Give the extent of all Plasmodium malariae-infected red blood cells.
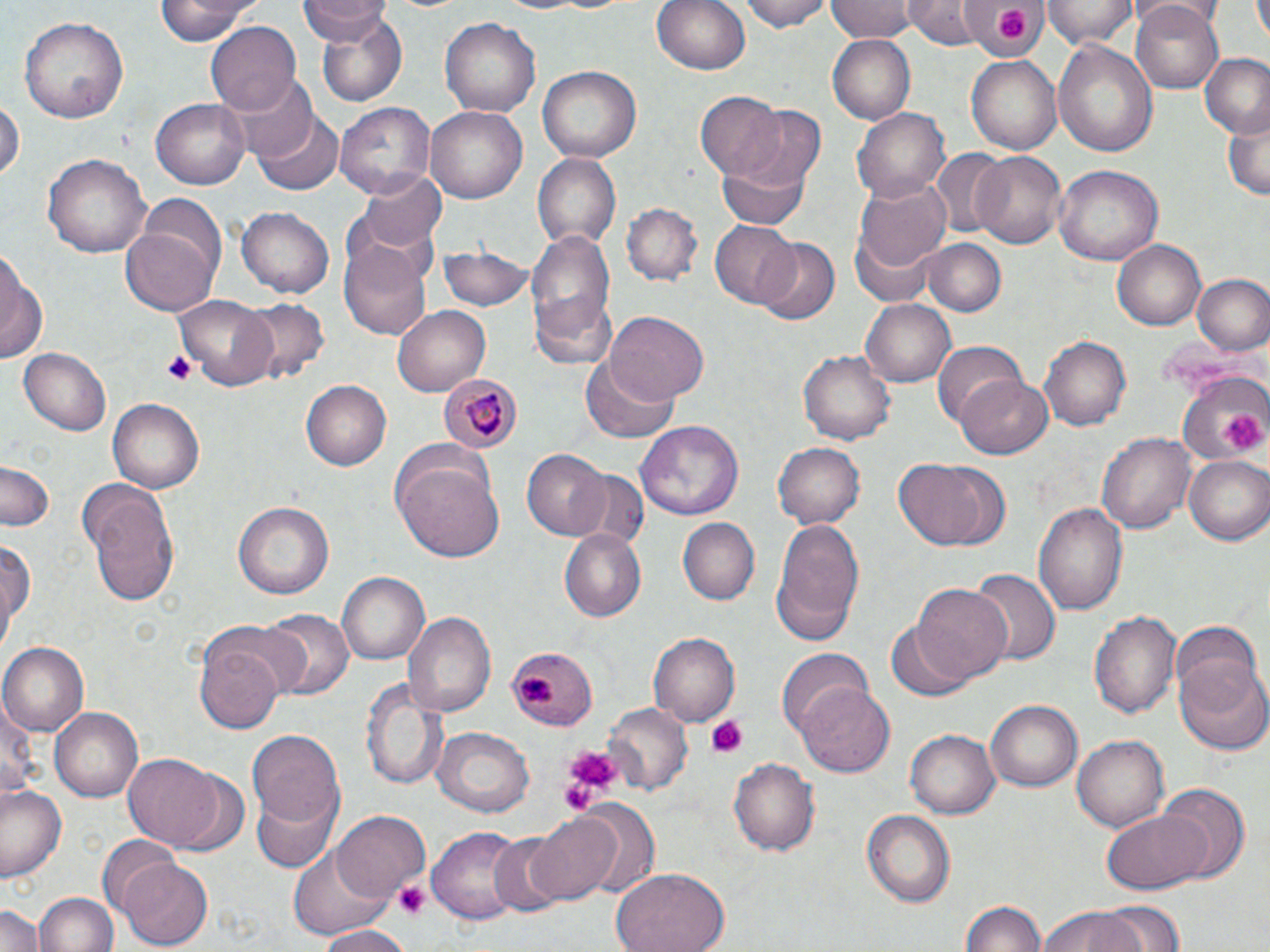
Approximate bounding boxes as [x1, y1, x2, y2] in pixels.
Plasmodium malariae-infected red blood cells: [441, 371, 521, 455].

Platelet locations: [992, 6, 1028, 43], [161, 350, 195, 386], [1220, 409, 1266, 454], [516, 674, 559, 711], [704, 716, 748, 757], [561, 744, 619, 797], [558, 764, 606, 816], [395, 882, 428, 920]. Uninfected red blood cell locations: [154, 0, 263, 46], [298, 0, 389, 41], [654, 0, 752, 76], [741, 0, 833, 31], [826, 0, 916, 43], [906, 0, 982, 46], [1043, 0, 1135, 49], [959, 2, 1050, 60], [1252, 2, 1270, 41], [1132, 3, 1224, 91], [313, 10, 407, 108], [19, 14, 128, 124], [441, 18, 540, 117], [207, 20, 304, 117], [827, 37, 915, 122], [1053, 40, 1159, 156], [1198, 53, 1270, 140], [967, 54, 1063, 154], [539, 65, 643, 163], [235, 76, 319, 167], [697, 91, 785, 178], [0, 95, 23, 186], [151, 95, 250, 188], [337, 103, 435, 200], [736, 104, 828, 188], [425, 105, 530, 205], [852, 106, 949, 204], [252, 109, 342, 196], [1222, 116, 1270, 202], [928, 149, 1009, 237], [974, 151, 1067, 249], [42, 153, 153, 259], [533, 154, 621, 249], [717, 154, 811, 229], [1052, 165, 1163, 266], [361, 169, 447, 254], [860, 178, 949, 273], [137, 194, 229, 283], [623, 201, 700, 285], [235, 205, 335, 298], [120, 219, 219, 315], [709, 220, 801, 306], [853, 220, 939, 311], [524, 228, 617, 365], [340, 238, 433, 339], [756, 238, 839, 324], [923, 239, 1004, 314], [1113, 240, 1206, 331], [443, 243, 531, 314], [0, 254, 47, 370], [1192, 274, 1270, 355], [175, 293, 279, 391], [236, 297, 330, 389], [863, 299, 955, 387], [393, 305, 490, 395], [606, 312, 709, 407], [1039, 336, 1131, 431], [933, 342, 1027, 429], [19, 347, 112, 435], [800, 348, 895, 442], [583, 355, 681, 442], [1180, 372, 1266, 467], [958, 374, 1054, 458], [301, 380, 391, 470], [107, 398, 206, 494], [636, 420, 745, 522], [1099, 431, 1196, 533], [772, 441, 865, 529], [521, 449, 609, 539], [1184, 456, 1270, 546], [896, 459, 993, 551], [396, 460, 503, 561], [0, 462, 55, 532], [572, 471, 645, 547], [85, 483, 182, 606], [232, 501, 335, 601], [1034, 502, 1128, 615], [771, 516, 865, 645], [678, 517, 758, 605], [560, 530, 646, 622], [0, 539, 35, 652], [969, 568, 1062, 665], [337, 572, 429, 664], [913, 584, 1011, 683], [1089, 608, 1181, 720], [260, 609, 353, 700], [405, 610, 497, 718], [1169, 621, 1261, 707], [887, 622, 968, 703], [192, 624, 292, 734], [648, 632, 740, 726], [1, 644, 87, 736], [505, 646, 596, 729], [779, 650, 875, 737], [1176, 656, 1270, 756], [360, 677, 445, 790], [797, 686, 896, 778], [0, 701, 44, 797], [987, 701, 1082, 791], [601, 704, 690, 794], [51, 706, 148, 802], [248, 728, 343, 825], [434, 728, 534, 817], [906, 729, 999, 819], [1072, 734, 1168, 832], [124, 754, 225, 847], [728, 756, 818, 857], [168, 770, 252, 860], [2, 783, 67, 882], [1156, 785, 1250, 884], [251, 787, 341, 872], [570, 799, 660, 899], [1103, 807, 1210, 895], [526, 809, 626, 903], [332, 811, 430, 900], [863, 811, 957, 908], [428, 826, 527, 923], [489, 835, 571, 918], [96, 838, 180, 920], [290, 846, 396, 938], [117, 857, 213, 949], [610, 867, 730, 952], [33, 892, 118, 952], [960, 900, 1047, 952], [1097, 900, 1187, 951], [0, 901, 45, 952], [1039, 907, 1144, 952], [314, 924, 410, 952]. Slide-level diagnosis: Plasmodium malariae. Thin blood film. Captured at 1000x magnification. Single field of view. Light microscopy. Image is 1270×952 pixels. May-Grünwald-Giemsa stain.